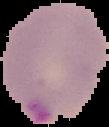 Result: Plasmodium parasites identified. Cell region segmented out of the field of view; the surrounding area is masked to black. Image is 109×127 pixels. From a thin blood smear.